Locate every leukocyte (white blood cell).
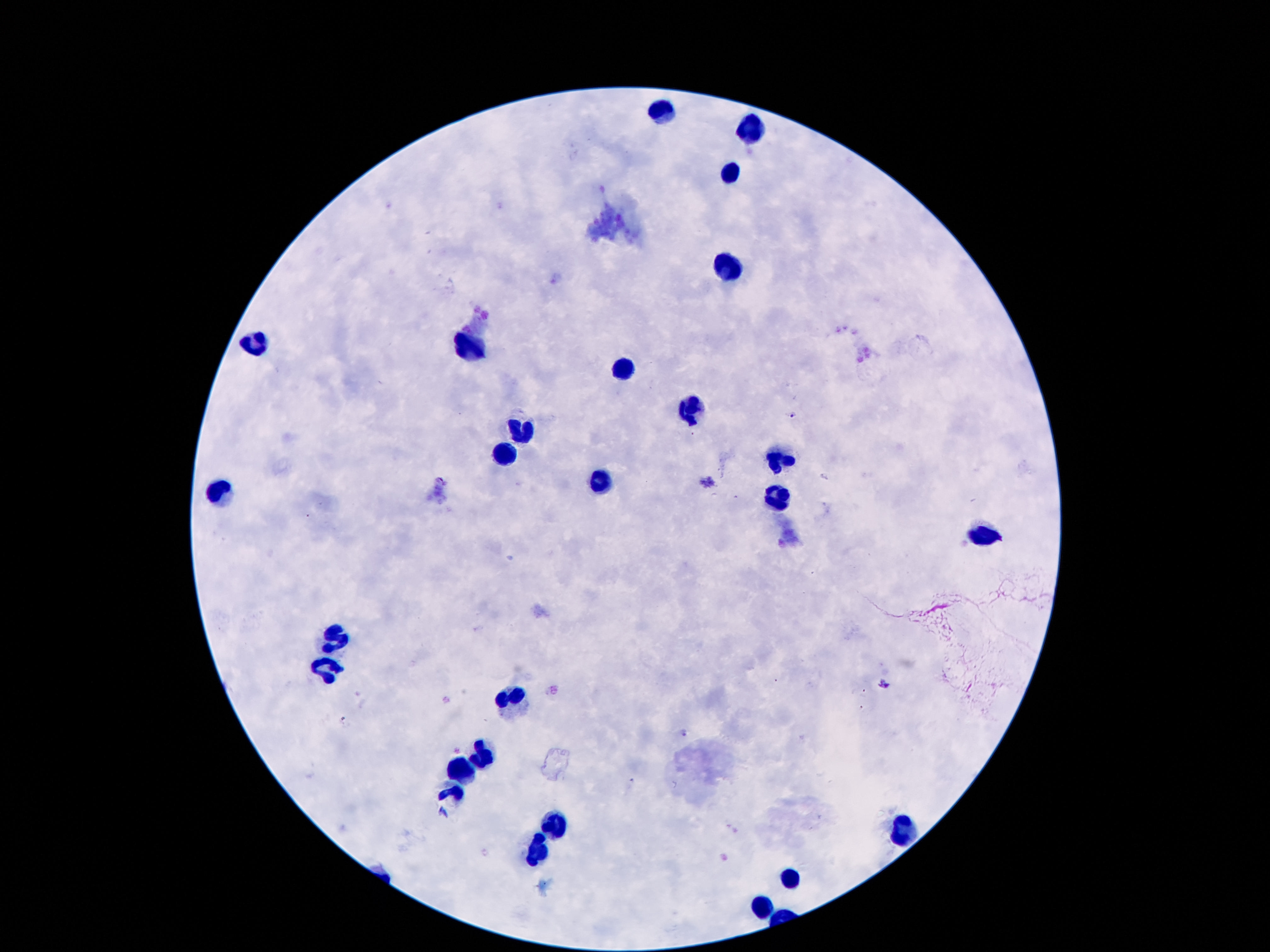

Approximate centers as (x, y) in pixels.
Leukocytes: (661, 108), (752, 129), (731, 172), (724, 267), (256, 337), (468, 348), (626, 367), (693, 413), (523, 430), (506, 451), (781, 458), (601, 483), (223, 489), (777, 499), (983, 537), (334, 644), (328, 667), (514, 699), (483, 758), (462, 772), (454, 795), (554, 828), (903, 829), (535, 850), (787, 875), (762, 908).

Summary:
  - Stain: Giemsa
  - Image size: 1270×952 pixels
  - Field of view: one from this slide
  - Preparation: thick blood smear
  - Patient malaria status: uninfected
  - Capture: smartphone camera through the microscope eyepiece
  - Magnification: 100x